Name the blood parasite species.
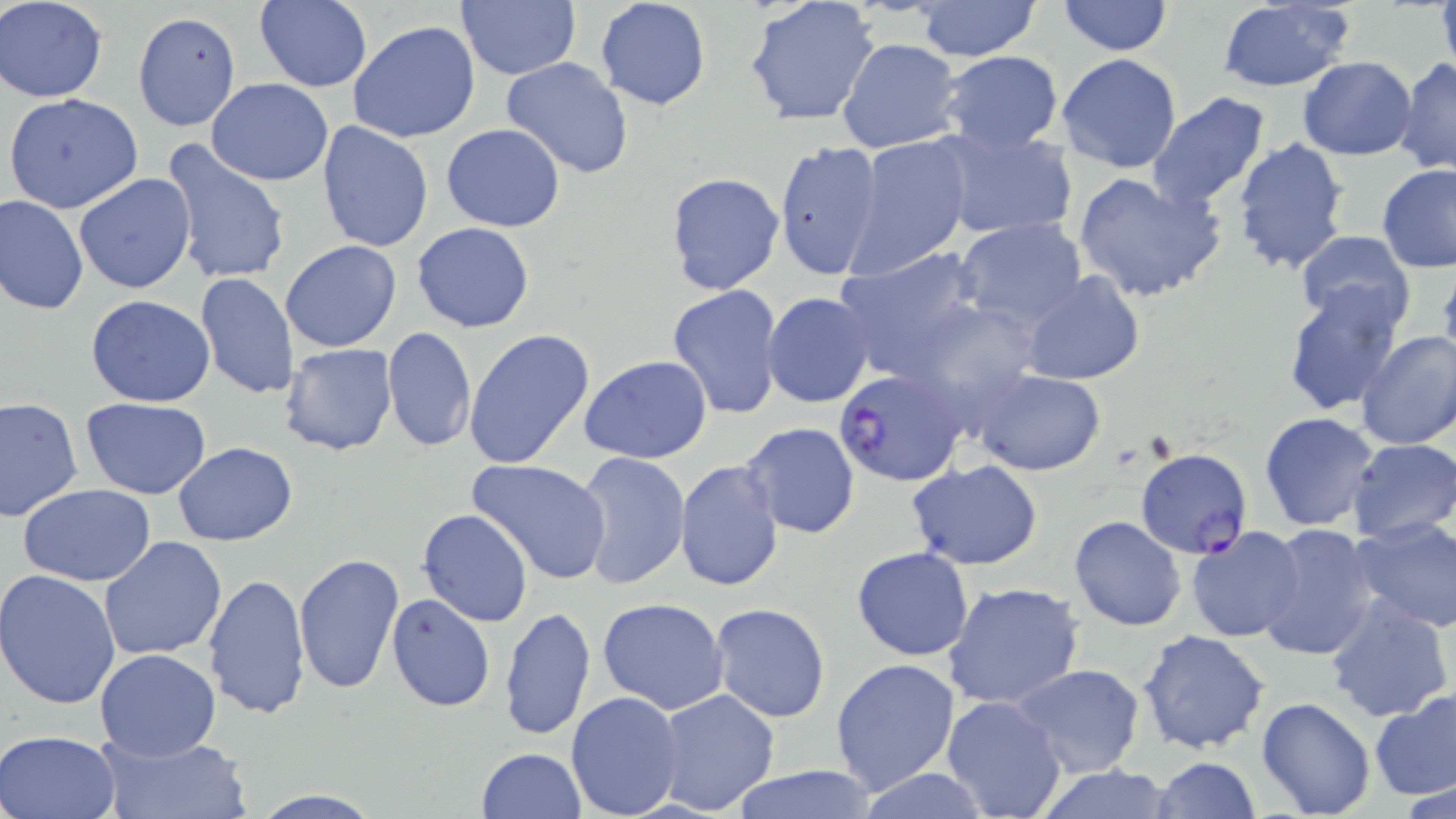
Plasmodium falciparum.

Approximate bounding boxes as (x1, y1, x2, y2) in pixels. Plasmodium falciparum-infected red blood cell locations: (834, 369, 967, 486), (1134, 448, 1252, 558). Uninfected red blood cell locations: (457, 0, 581, 80), (594, 0, 710, 111), (3, 1, 108, 102), (253, 1, 373, 91), (743, 1, 880, 125), (912, 1, 1041, 61), (1057, 1, 1174, 56), (1433, 1, 1455, 78), (1214, 2, 1357, 92), (131, 11, 240, 131), (347, 21, 481, 143), (837, 37, 961, 154), (938, 50, 1064, 154), (1057, 53, 1182, 174), (1298, 55, 1418, 160), (1394, 56, 1456, 176), (501, 57, 634, 178), (206, 78, 333, 185), (1146, 92, 1274, 210), (3, 93, 143, 212), (316, 120, 433, 253), (442, 124, 566, 232), (933, 127, 1074, 242), (846, 135, 973, 277), (1231, 136, 1352, 274), (159, 139, 291, 288), (773, 141, 881, 280), (1376, 163, 1456, 272), (1071, 171, 1227, 305), (663, 172, 785, 296), (73, 173, 197, 294), (1, 194, 88, 316), (954, 218, 1089, 335), (411, 223, 536, 333), (1294, 231, 1418, 336), (280, 240, 401, 352), (834, 248, 987, 380), (1438, 267, 1456, 374), (1021, 271, 1145, 386), (195, 273, 297, 399), (1281, 283, 1406, 415), (667, 284, 784, 419), (762, 293, 874, 408), (85, 295, 216, 407), (382, 326, 476, 453), (464, 328, 596, 471), (1355, 329, 1456, 451), (282, 342, 399, 455), (579, 355, 712, 463), (972, 368, 1107, 476), (0, 395, 83, 524), (81, 396, 211, 499), (1259, 412, 1379, 531), (739, 420, 861, 539), (1346, 438, 1456, 544), (172, 442, 297, 546), (576, 451, 690, 590), (675, 457, 783, 592), (465, 458, 614, 587), (906, 460, 1044, 568), (18, 483, 157, 587), (417, 509, 533, 628), (1069, 515, 1187, 632), (1350, 516, 1456, 633), (1256, 524, 1381, 663), (1186, 526, 1304, 643), (99, 536, 229, 661), (851, 547, 974, 662), (294, 552, 404, 694), (0, 570, 122, 708), (202, 571, 311, 721), (943, 581, 1084, 710), (1324, 589, 1455, 722), (387, 592, 496, 712), (596, 598, 729, 715), (708, 602, 831, 723), (499, 605, 596, 743), (1138, 628, 1270, 754), (94, 647, 221, 759), (832, 657, 962, 796), (1011, 664, 1145, 778), (654, 689, 782, 814), (566, 690, 685, 817), (1370, 691, 1455, 801), (941, 694, 1068, 819), (1256, 697, 1376, 818), (1, 729, 122, 818), (95, 731, 250, 819), (475, 747, 586, 819), (1150, 757, 1261, 818), (1028, 764, 1174, 818), (728, 765, 879, 819), (850, 768, 989, 819), (248, 790, 389, 818). Thin blood smear. Single field of view. May-Grünwald-Giemsa-stained preparation. Captured at 1000x magnification. Light microscopy. Image is 1456×819 pixels.